Classify this cell by malaria status.
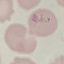
Uninfected.

stain = Giemsa
image type = automatically extracted cell patch, resized to 64 × 64 pixels
capture = smartphone camera at the microscope eyepiece
preparation = thin smear